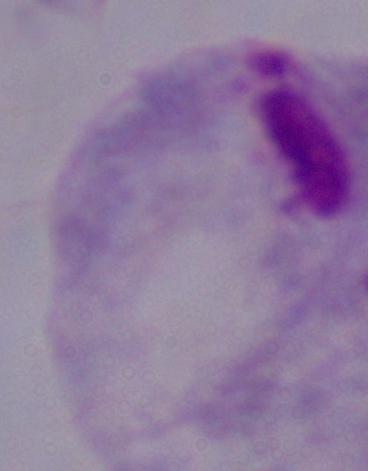

Summary:
  - Magnification: 1000x
  - Identification: trichomonad
  - Modality: micrograph